Identify the blood parasite species.
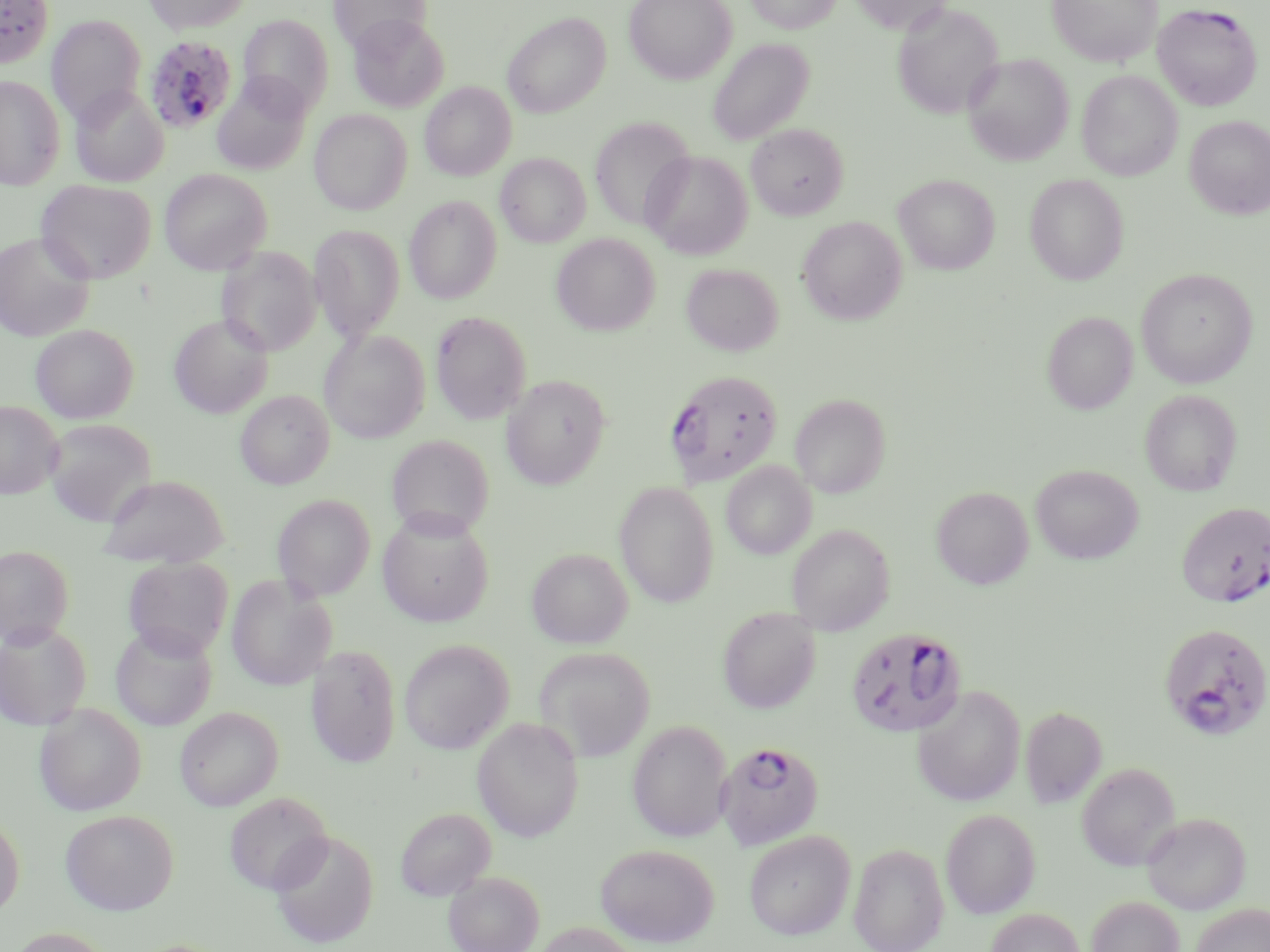

Plasmodium falciparum.

uninfected red blood cell locations = approximate bounding boxes as [x1, y1, x2, y2] in pixels: [141, 0, 253, 34], [328, 0, 431, 53], [623, 0, 736, 84], [743, 0, 842, 34], [847, 0, 953, 33], [1047, 0, 1163, 66], [892, 2, 1004, 120], [503, 12, 610, 117], [238, 13, 333, 117], [47, 14, 147, 124], [348, 14, 449, 112], [707, 38, 814, 145], [962, 53, 1073, 165], [1077, 70, 1183, 180], [212, 74, 312, 175], [0, 75, 65, 189], [420, 81, 516, 181], [69, 84, 168, 187], [309, 109, 412, 215], [1184, 115, 1270, 219], [589, 116, 696, 231], [745, 124, 848, 220], [642, 151, 752, 259], [495, 152, 591, 247], [160, 168, 272, 274], [1024, 173, 1129, 285], [893, 174, 1000, 274], [36, 179, 156, 284], [404, 195, 501, 303], [797, 216, 907, 325], [309, 225, 404, 342], [0, 232, 95, 341], [551, 233, 659, 336], [217, 246, 322, 357], [680, 262, 784, 356], [1135, 267, 1257, 388], [431, 310, 532, 424], [1042, 311, 1138, 414], [169, 313, 273, 418], [31, 324, 138, 423], [319, 328, 430, 443], [501, 375, 611, 489], [235, 389, 335, 489], [1140, 389, 1242, 496], [790, 393, 890, 498], [0, 401, 62, 499], [44, 418, 156, 526], [386, 435, 494, 539], [721, 461, 816, 560], [1030, 464, 1144, 564], [98, 473, 230, 567], [614, 481, 718, 608], [931, 486, 1033, 590], [272, 494, 375, 601], [377, 511, 494, 627], [786, 523, 894, 635], [0, 545, 74, 647], [526, 548, 633, 649], [123, 557, 234, 658], [226, 574, 337, 691], [717, 606, 821, 714], [0, 621, 92, 730], [110, 623, 218, 731], [399, 639, 513, 754], [306, 644, 402, 768], [534, 646, 656, 762], [913, 685, 1026, 807], [33, 702, 147, 816], [175, 706, 283, 811], [1020, 706, 1107, 809], [472, 716, 585, 842], [628, 719, 733, 842], [1077, 763, 1180, 871], [224, 792, 333, 896], [395, 807, 495, 900], [60, 809, 179, 915], [940, 809, 1040, 918], [1141, 812, 1251, 914], [0, 813, 24, 919], [269, 829, 379, 948], [743, 830, 856, 940], [849, 842, 949, 952], [595, 843, 719, 947], [444, 870, 544, 952], [1086, 895, 1184, 952], [1190, 903, 1270, 952], [985, 908, 1085, 952], [533, 921, 641, 952], [7, 927, 115, 952]
Plasmodium falciparum-infected red blood cell locations = approximate bounding boxes as [x1, y1, x2, y2] in pixels: [0, 0, 54, 67], [1153, 3, 1262, 110], [143, 34, 237, 134], [664, 369, 784, 486], [1177, 501, 1270, 607], [1158, 622, 1270, 741], [845, 627, 968, 738], [716, 740, 825, 850]
magnification = 1000x
image size = 1270×952 pixels
stain = May-Grünwald-Giemsa
modality = light microscopy
preparation = thin blood film
field of view = single